Assess this cell for malaria.
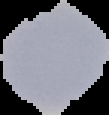
It is uninfected.

{
  "image_type": "segmented cell region with the area outside set to black",
  "image_size": "109×115 pixels",
  "preparation": "thin blood smear"
}